Point out each malaria parasite.
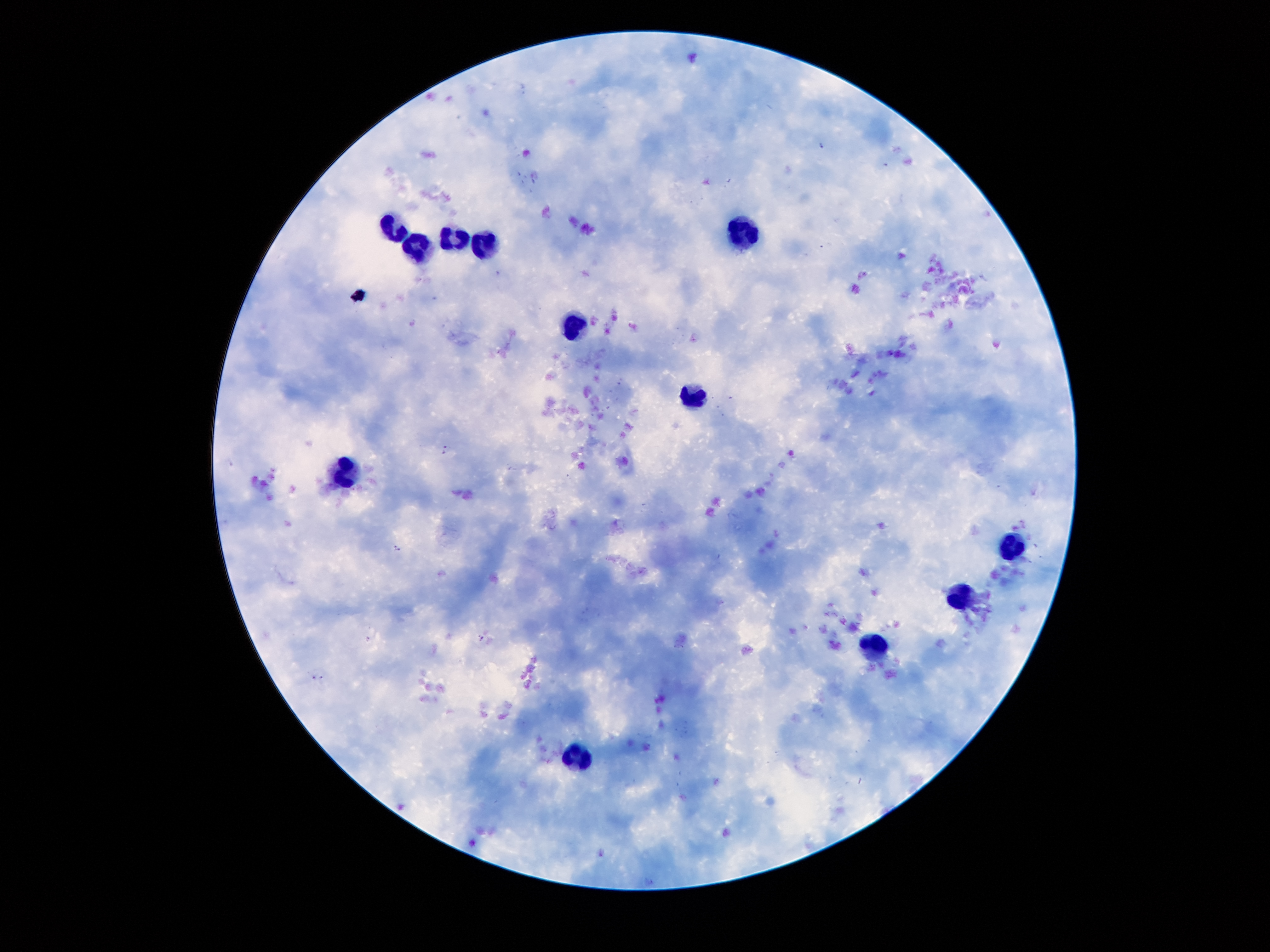
Approximate centers as {x, y} in pixels.
Malaria parasites: {446, 450}, {396, 548}, {482, 639}, {318, 678}.

leukocyte locations = {745, 229}, {399, 230}, {453, 238}, {485, 244}, {422, 250}, {574, 322}, {697, 393}, {342, 474}, {1014, 548}, {961, 598}, {874, 649}, {577, 751}
stain = Giemsa
patient malaria status = infected with Plasmodium falciparum
magnification = 100x
capture = smartphone through the microscope eyepiece
preparation = thick peripheral-blood smear
field of view = single
image size = 1270×952 pixels